Evaluate for malaria.
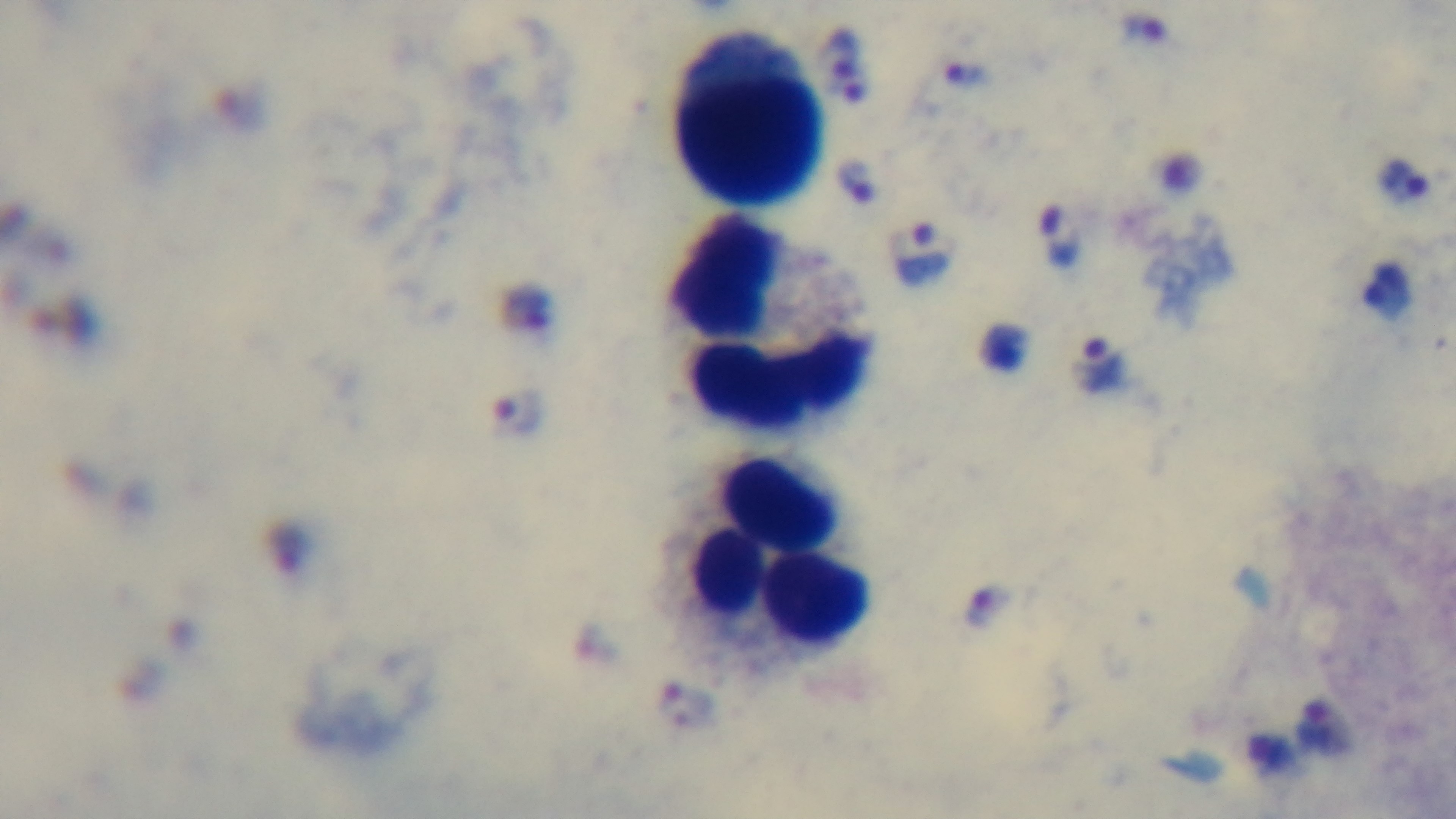
It is infected.

Summary:
  - Stain: Giemsa
  - Capture: mounted 4K digital camera
  - Modality: light microscopy
  - Preparation: thick smear
  - Field of view: one from the slide
  - Objective: 100x oil immersion